Classify this cell by malaria status.
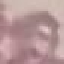
Uninfected.

stain: Giemsa
capture: smartphone camera at the microscope eyepiece
preparation: thin smear
image_type: cell patch, automatically extracted from a larger field of view and resized to 64 × 64 pixels